State which parasite is depicted.
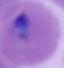
Plasmodium.

Summary:
  - Modality: photomicrograph
  - Magnification: 400x or 1000x